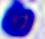
Summary:
  - Identification: white blood cell
  - Modality: photomicrograph
  - Magnification: 400x